Give the position of every leukocyte visible.
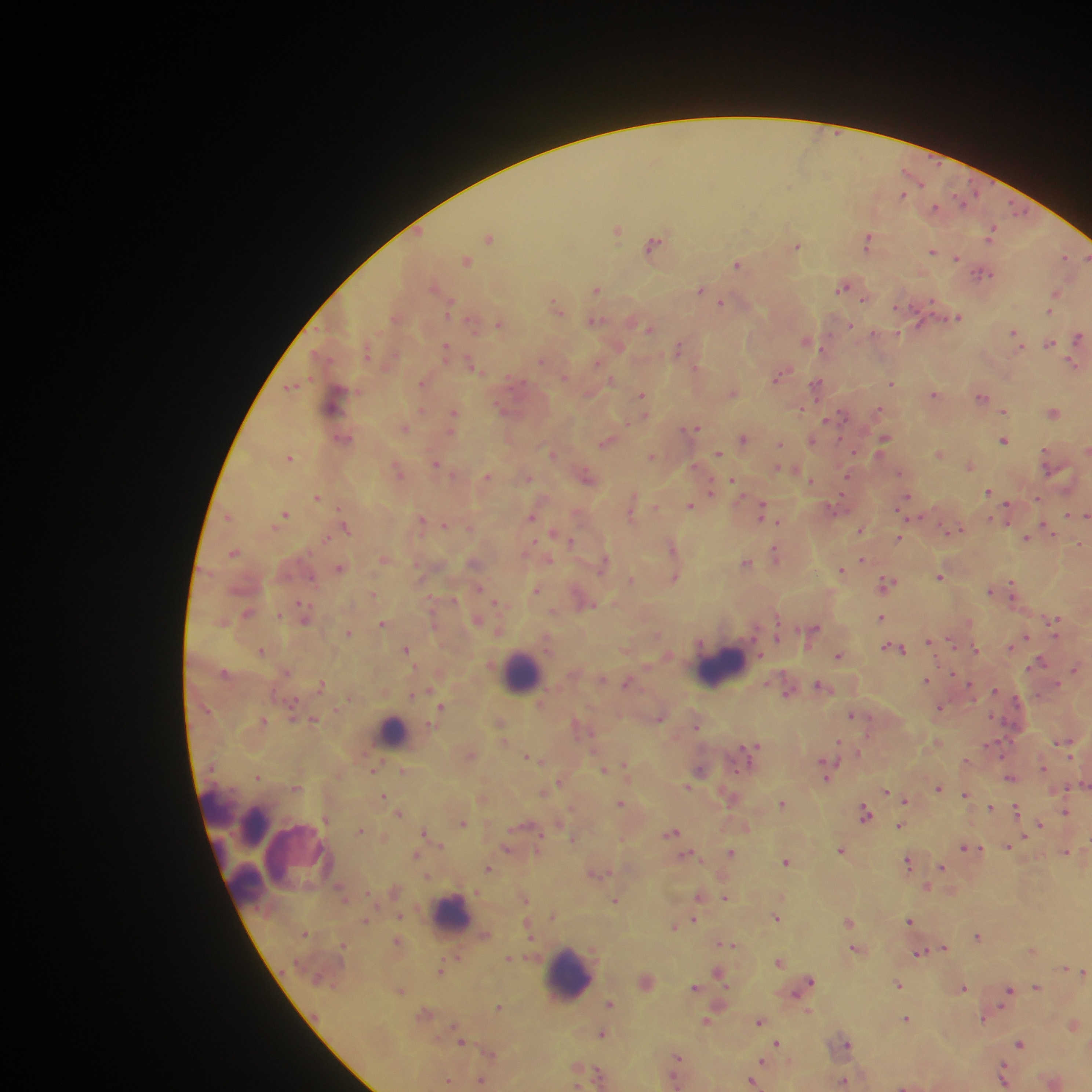

Approximate centers as x y in pixels.
Leukocytes: 720 665; 521 673; 393 731; 218 805; 250 819; 295 851; 244 893; 451 914; 567 974.

country: Ghana
plasmodium_parasite_locations: 'approximate centers as x y in pixels: 902 195; 963 200; 935 206; 1018 210; 617 230; 991 234; 490 237; 867 241; 653 244; 797 247; 933 252; 1064 257; 956 258; 1086 258; 466 261; 738 265; 982 273; 842 287; 597 289; 700 289; 1056 293; 864 300; 721 304; 450 306; 899 306; 557 308; 1050 312; 957 318; 596 321; 499 324; 918 324; 850 326; 649 329; 873 333; 1014 334; 1078 337; 806 341; 1049 343; 446 347; 678 348; 541 360; 597 362; 1073 365; 474 367; 565 376; 777 377; 611 380; 422 383; 893 383; 817 384; 292 387; 733 392; 642 394; 934 394; 982 396; 335 398; 500 406; 800 409; 878 409; 422 411; 1003 411; 1053 413; 454 414; 842 416; 827 419; 405 427; 695 428; 743 438; 346 439; 884 439; 812 441; 1003 441; 606 443; 780 444; 1087 450; 550 452; 718 453; 940 454; 652 455; 290 457; 436 464; 970 465; 779 469; 398 470; 900 473; 587 476; 487 477; 812 480; 846 481; 734 482; 711 489; 989 492; 317 497; 906 498; 633 499; 1038 499; 690 506; 1007 510; 762 511; 285 514; 1068 514; 531 516; 1085 516; 991 519; 421 521; 778 522; 445 525; 1046 526; 346 527; 860 530; 957 530; 554 532; 899 537; 326 538; 1026 538; 573 542; 672 546; 234 553; 776 554; 862 560; 746 563; 603 566; 340 569; 840 570; 940 576; 675 577; 312 578; 887 583; 1013 588; 990 590; 536 591; 497 603; 589 605; 303 611; 279 615; 881 617; 305 618; 1055 621; 382 623; 813 630; 349 632; 658 634; 778 637; 1025 637; 950 640; 929 641; 890 648; 407 649; 900 649; 975 650; 261 651; 839 656; 1039 662; 1074 668; 927 680; 626 683; 1056 684; 321 685; 820 686; 969 686; 995 691; 414 694; 787 694; 1017 701; 442 708; 941 708; 292 712; 852 715; 661 718; 314 720; 263 721; 697 726; 1065 743; 838 745; 752 746; 470 754; 528 757; 1043 768; 375 769; 700 769; 403 770; 604 770; 827 771; 258 776; 1009 777; 560 782; 296 787; 688 787; 938 788; 886 791; 966 794; 383 797; 905 800; 620 803; 783 804; 990 807; 1016 810; 1066 810; 400 813; 865 813; 463 822; 900 825; 1040 825; 361 830; 425 831; 672 831; 574 838; 1008 846; 507 847; 965 847; 841 850; 731 852; 1065 852; 416 855; 688 855; 786 862; 908 862; 941 867; 488 868; 595 873; 926 888; 698 897; 725 898; 525 900; 615 901; 777 917; 366 920; 696 920; 909 920; 848 921; 675 926; 977 937; 728 944; 943 948; 854 949; 1031 950; 920 953; 457 955; 508 959; 779 962; 1065 968; 440 970; 1084 972; 718 973; 809 981; 898 985; 694 987; 963 987; 1037 987; 1009 990; 402 991; 610 1004; 499 1007; 906 1018; 983 1018; 706 1021; 759 1022; 1073 1025; 601 1034; 462 1042; 777 1043; 1020 1043; 846 1044; 677 1057; 762 1061; 598 1074; 1003 1077; 448 1081; 481 1081; 844 1081; 752 1082'
field_of_view: single
preparation: thick blood film
image_size: 1092×1092 pixels
capture: mobile-phone photograph through a microscope